State which parasite is depicted.
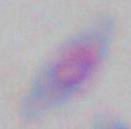

Toxoplasma gondii.

magnification: 1000x
modality: photomicrograph